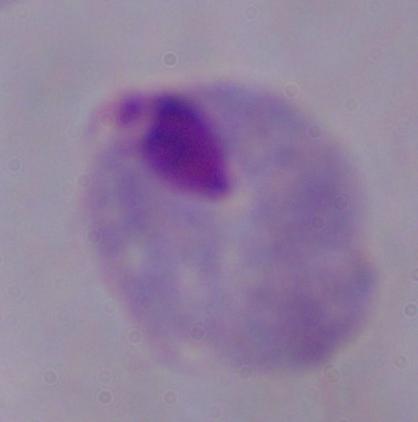

{
  "modality": "micrograph",
  "magnification": "1000x",
  "identification": "trichomonad"
}